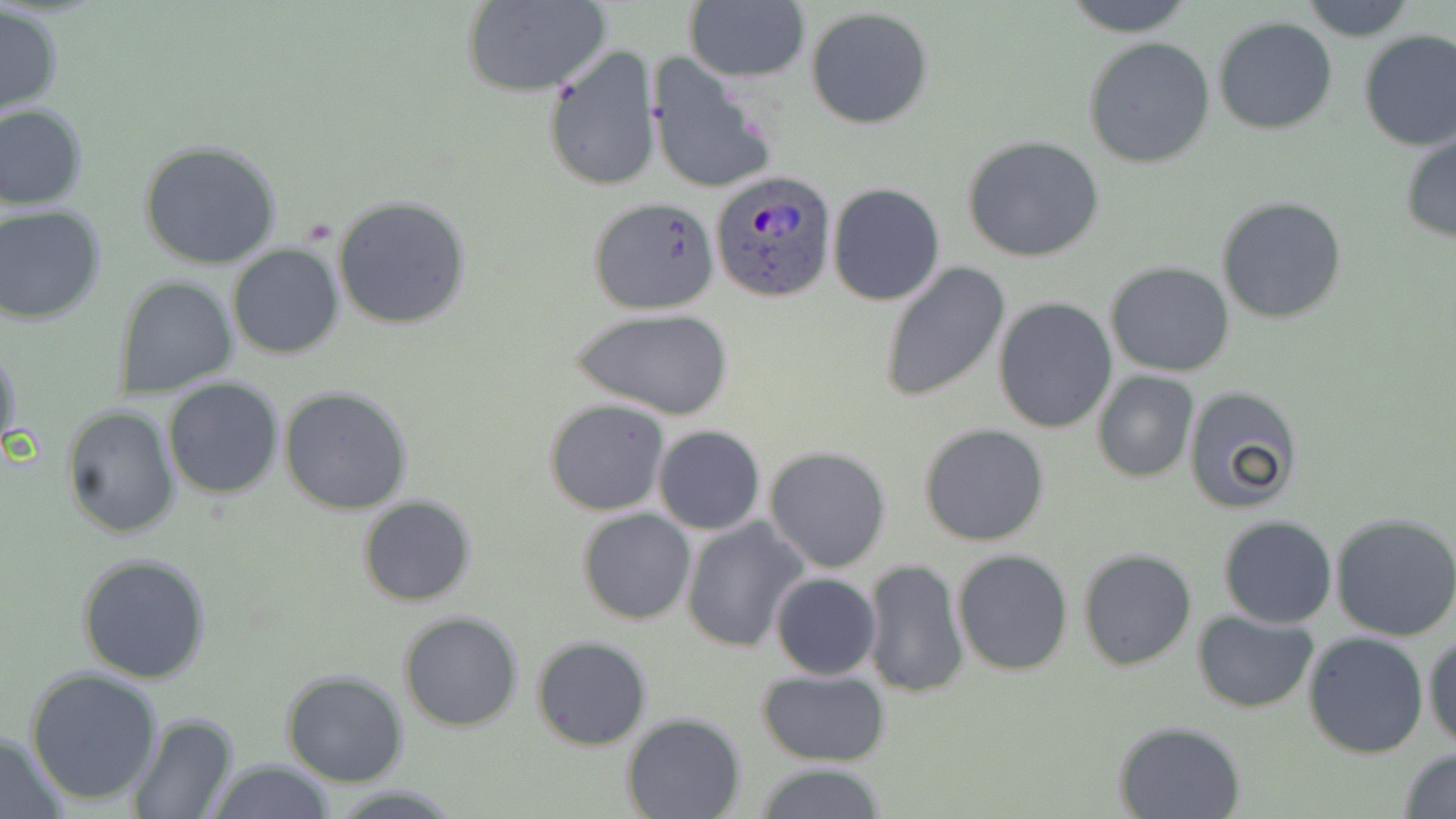
Approximate bounding boxes as [x1, y1, x2, y2] in pixels. Plasmodium ovale-infected red blood cell locations: [710, 169, 837, 301]. Uninfected red blood cell locations: [1057, 0, 1200, 38], [1295, 0, 1420, 42], [459, 1, 610, 97], [682, 1, 810, 84], [1, 5, 65, 119], [805, 7, 934, 129], [1212, 17, 1338, 136], [1356, 29, 1456, 154], [1084, 36, 1215, 168], [544, 47, 662, 193], [648, 55, 780, 197], [0, 103, 89, 210], [1399, 129, 1456, 243], [962, 134, 1105, 263], [138, 140, 283, 269], [827, 183, 945, 305], [333, 196, 471, 330], [1217, 196, 1348, 323], [587, 199, 719, 316], [0, 206, 106, 323], [227, 244, 344, 361], [878, 261, 1011, 402], [1105, 262, 1235, 377], [116, 275, 239, 398], [992, 298, 1117, 434], [571, 308, 735, 421], [0, 339, 21, 457], [1092, 371, 1199, 483], [162, 378, 284, 499], [1182, 385, 1305, 514], [279, 386, 412, 515], [543, 399, 673, 517], [62, 403, 181, 538], [919, 423, 1051, 547], [652, 426, 766, 535], [764, 445, 891, 573], [357, 495, 478, 606], [577, 509, 697, 625], [1332, 514, 1456, 642], [1218, 515, 1336, 628], [680, 517, 809, 652], [1079, 548, 1197, 671], [952, 550, 1073, 676], [77, 553, 211, 684], [862, 559, 969, 700], [770, 572, 880, 680], [1193, 609, 1320, 712], [398, 610, 525, 733], [1302, 630, 1431, 758], [1424, 632, 1456, 747], [532, 635, 652, 749], [24, 666, 164, 806], [757, 668, 890, 767], [282, 671, 407, 788], [127, 712, 236, 819], [621, 714, 746, 819], [1113, 720, 1245, 818], [0, 734, 71, 817], [1397, 747, 1456, 819], [204, 758, 335, 818], [751, 762, 889, 819], [325, 784, 465, 817]. Slide-level diagnosis: Plasmodium ovale. Thin blood smear. Image is 1456×819 pixels. Single field of view. May-Grünwald-Giemsa stain. Light microscopy. Captured at 1000x magnification.